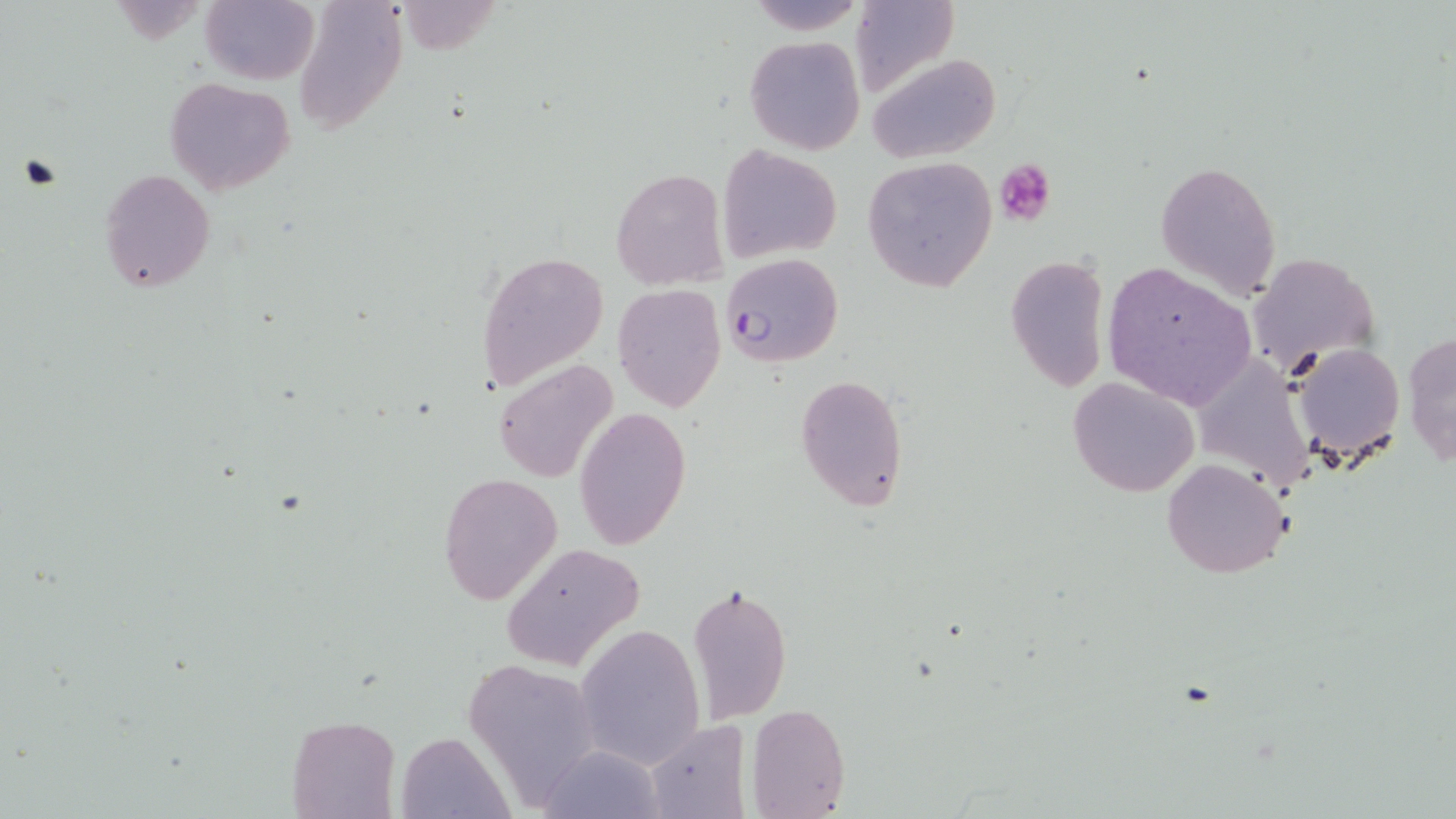

Summary:
  - Coordinate format: approximate bounding boxes as named x1/y1/x2/y2 corners in pixels
  - Uninfected red blood cell locations: (x1=201, y1=0, x2=320, y2=85), (x1=745, y1=0, x2=866, y2=35), (x1=295, y1=1, x2=408, y2=133), (x1=850, y1=1, x2=959, y2=97), (x1=744, y1=35, x2=865, y2=156), (x1=868, y1=53, x2=1000, y2=164), (x1=164, y1=76, x2=295, y2=194), (x1=719, y1=145, x2=842, y2=259), (x1=863, y1=157, x2=996, y2=291), (x1=1155, y1=160, x2=1281, y2=301), (x1=99, y1=169, x2=215, y2=293), (x1=612, y1=169, x2=727, y2=290), (x1=473, y1=250, x2=609, y2=393), (x1=1248, y1=251, x2=1381, y2=375), (x1=1006, y1=253, x2=1111, y2=392), (x1=1103, y1=261, x2=1257, y2=408), (x1=612, y1=283, x2=726, y2=412), (x1=1402, y1=330, x2=1456, y2=470), (x1=1288, y1=340, x2=1407, y2=465), (x1=1191, y1=355, x2=1316, y2=491), (x1=493, y1=359, x2=617, y2=483), (x1=794, y1=373, x2=909, y2=510), (x1=1067, y1=376, x2=1200, y2=497), (x1=574, y1=406, x2=691, y2=550), (x1=1161, y1=457, x2=1293, y2=580), (x1=438, y1=472, x2=563, y2=605), (x1=499, y1=543, x2=644, y2=672), (x1=689, y1=581, x2=792, y2=720), (x1=575, y1=622, x2=707, y2=769), (x1=466, y1=657, x2=600, y2=801), (x1=748, y1=703, x2=850, y2=818), (x1=286, y1=715, x2=399, y2=819), (x1=645, y1=719, x2=751, y2=817), (x1=397, y1=731, x2=511, y2=817), (x1=537, y1=743, x2=666, y2=818)
  - Platelet locations: (x1=17, y1=151, x2=65, y2=192), (x1=995, y1=157, x2=1056, y2=227)
  - Plasmodium falciparum-infected red blood cell locations: (x1=721, y1=253, x2=843, y2=369)
  - Slide-level diagnosis: Plasmodium falciparum
  - Magnification: 1000x
  - Modality: light microscopy
  - Image size: 1456×819 pixels
  - Stain: May-Grünwald-Giemsa
  - Field of view: one of a larger specimen
  - Preparation: thin blood film